State the preparation type.
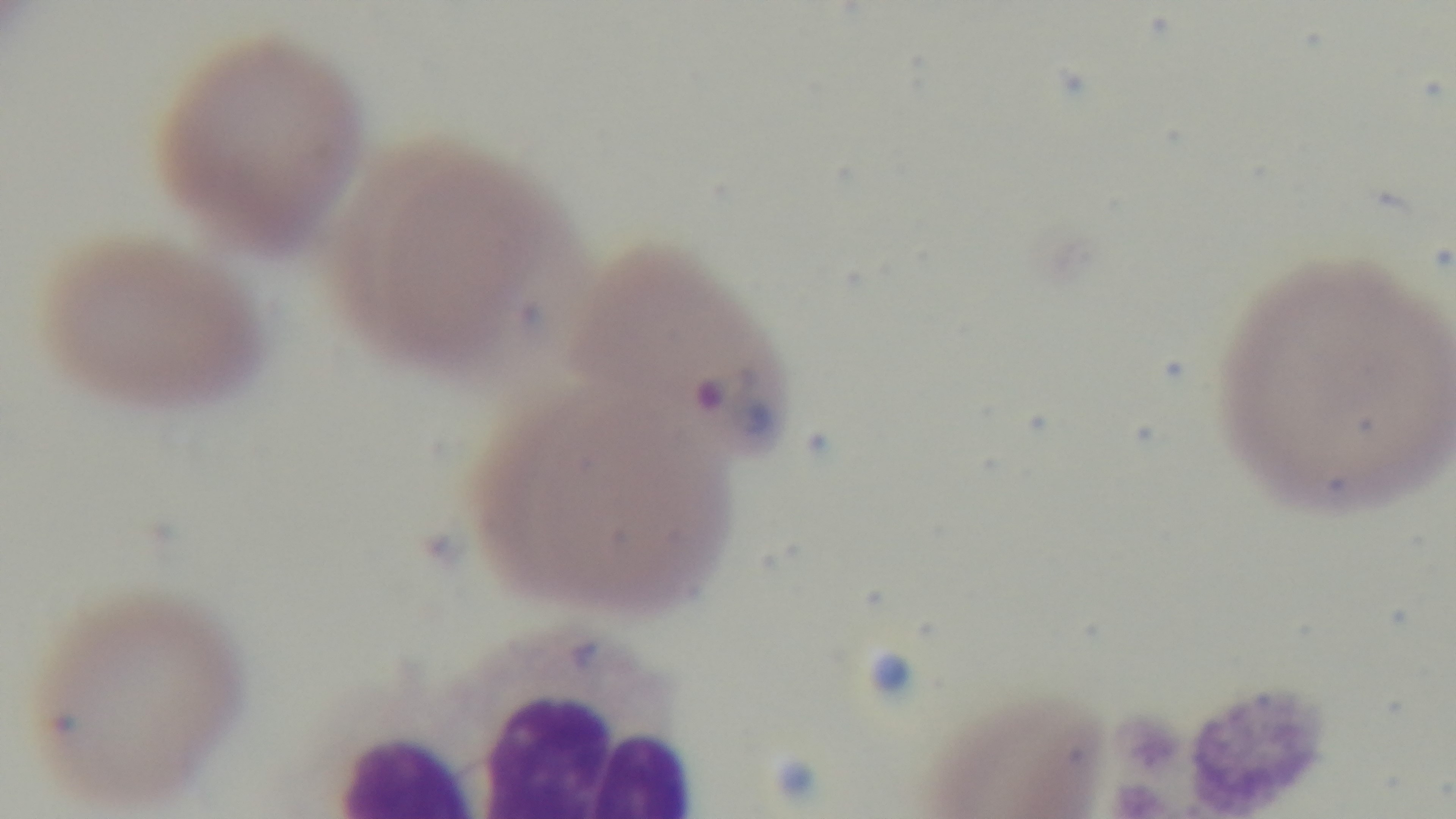
Thin.

stain = Giemsa
modality = light microscopy
field of view = single
malaria status = infected
capture = mounted 4K digital camera
objective = 100x oil immersion